Classify this cell by malaria status.
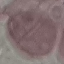

It is uninfected.

Giemsa-stained preparation. Thin blood smear. Acquired by smartphone through the microscope eyepiece. Automatically extracted cell patch, resized to 64 × 64 pixels.